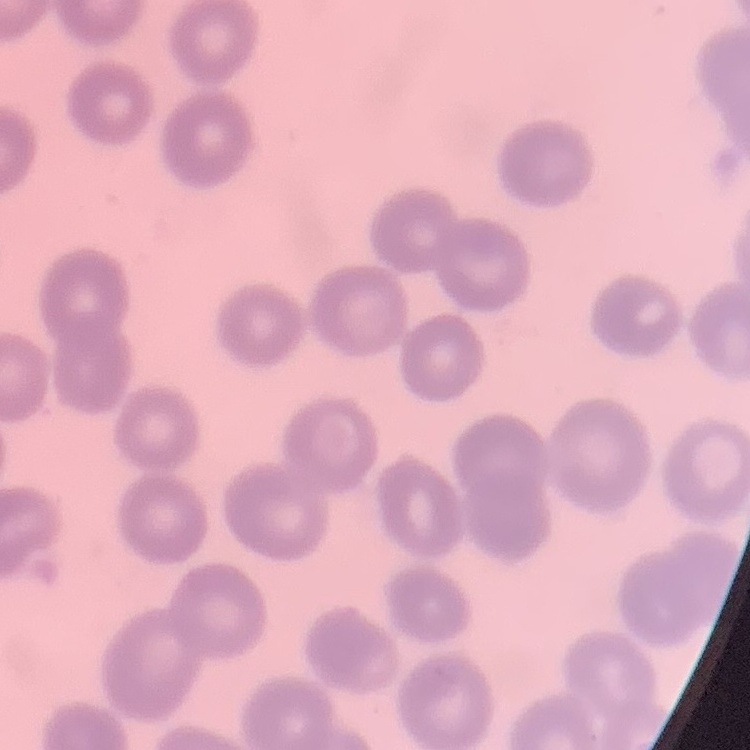

The erythrocytes exhibit no rouleaux formation. Field's or Giemsa stain. Square crop of a larger photomicrograph. Thin blood film.